State the blood parasite species.
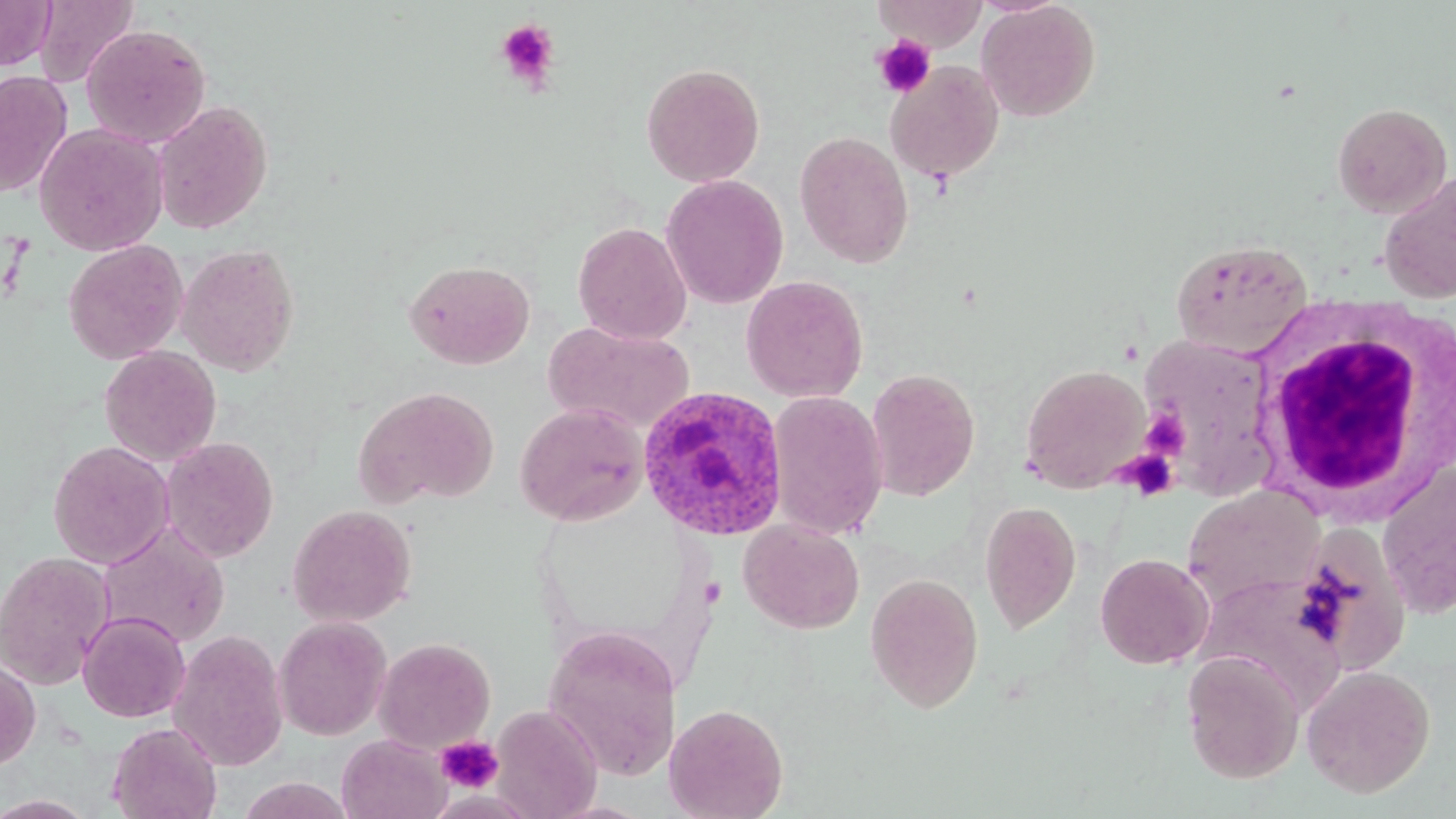

Plasmodium ovale.

uninfected red blood cell locations = approximate bounding boxes as [x1, y1, x2, y2] in pixels: [0, 0, 57, 70], [34, 0, 138, 87], [873, 0, 988, 52], [977, 0, 1101, 122], [81, 24, 211, 148], [885, 61, 1004, 184], [641, 62, 765, 187], [0, 70, 73, 197], [152, 100, 273, 235], [1331, 101, 1453, 218], [34, 122, 168, 256], [794, 130, 914, 267], [1379, 172, 1456, 303], [660, 174, 789, 309], [572, 222, 692, 344], [1170, 238, 1313, 358], [63, 239, 188, 365], [176, 243, 300, 376], [405, 258, 536, 369], [741, 275, 868, 402], [544, 320, 696, 434], [1135, 331, 1279, 496], [100, 346, 221, 465], [1020, 364, 1152, 493], [864, 368, 980, 501], [353, 386, 500, 508], [767, 390, 888, 542], [515, 402, 648, 526], [161, 437, 279, 562], [47, 440, 174, 569], [1377, 462, 1456, 619], [1182, 484, 1325, 611], [979, 500, 1081, 634], [287, 504, 417, 627], [738, 519, 865, 634], [98, 522, 230, 648], [1290, 522, 1412, 677], [0, 550, 114, 690], [1095, 552, 1214, 669], [864, 572, 984, 713], [77, 611, 191, 722], [274, 616, 392, 740], [543, 625, 683, 781], [169, 629, 288, 771], [374, 636, 496, 753], [1181, 649, 1305, 784], [0, 658, 41, 771], [1300, 664, 1436, 798], [664, 702, 788, 819], [490, 704, 602, 819], [106, 722, 223, 819], [337, 734, 451, 819], [236, 775, 352, 818], [0, 794, 97, 818]
magnification = 1000x
image size = 1456×819 pixels
stain = May-Grünwald-Giemsa
platelet locations = approximate bounding boxes as [x1, y1, x2, y2] in pixels: [494, 19, 561, 93], [872, 35, 936, 98], [1141, 408, 1188, 460], [1117, 451, 1180, 501], [435, 733, 504, 794]
modality = light microscopy
Plasmodium ovale-infected red blood cell locations = approximate bounding boxes as [x1, y1, x2, y2] in pixels: [637, 385, 790, 542]
field of view = single
preparation = thin blood smear
white blood cell locations = approximate bounding boxes as [x1, y1, x2, y2] in pixels: [1248, 304, 1454, 519]